Classify this cell by malaria status.
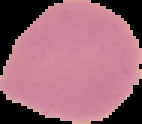

Uninfected.

Segmented cell region on a black background. From a thin blood smear. Image is 142×124 pixels.